State which cell type is depicted.
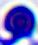
This is a leukocyte.

Summary:
  - Magnification: 400x
  - Modality: photomicrograph